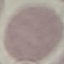 Result: no malaria parasites seen. Cell patch, automatically extracted from a larger field of view and resized to 64 × 64 pixels. Photographed with a smartphone camera at the microscope eyepiece. Giemsa-stained preparation. Thin smear of blood.